Report the malaria status of this cell.
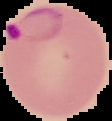

It is parasitized.

Segmented cell region on a black background. From a thin blood film. Image is 112×121 pixels.